Classify this cell by malaria status.
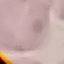
Uninfected.

{
  "image_type": "automatically extracted cell patch, resized to 64 × 64 pixels",
  "preparation": "thin smear",
  "capture": "smartphone through the microscope eyepiece",
  "stain": "Giemsa"
}